Classify this cell by malaria status.
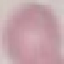

It is uninfected.

Summary:
  - Image type: cell patch, automatically extracted from a larger field of view and resized to 64 × 64 pixels
  - Stain: Giemsa
  - Preparation: thin blood smear
  - Capture: smartphone camera at the microscope eyepiece